Outline each blood parasite and name the species.
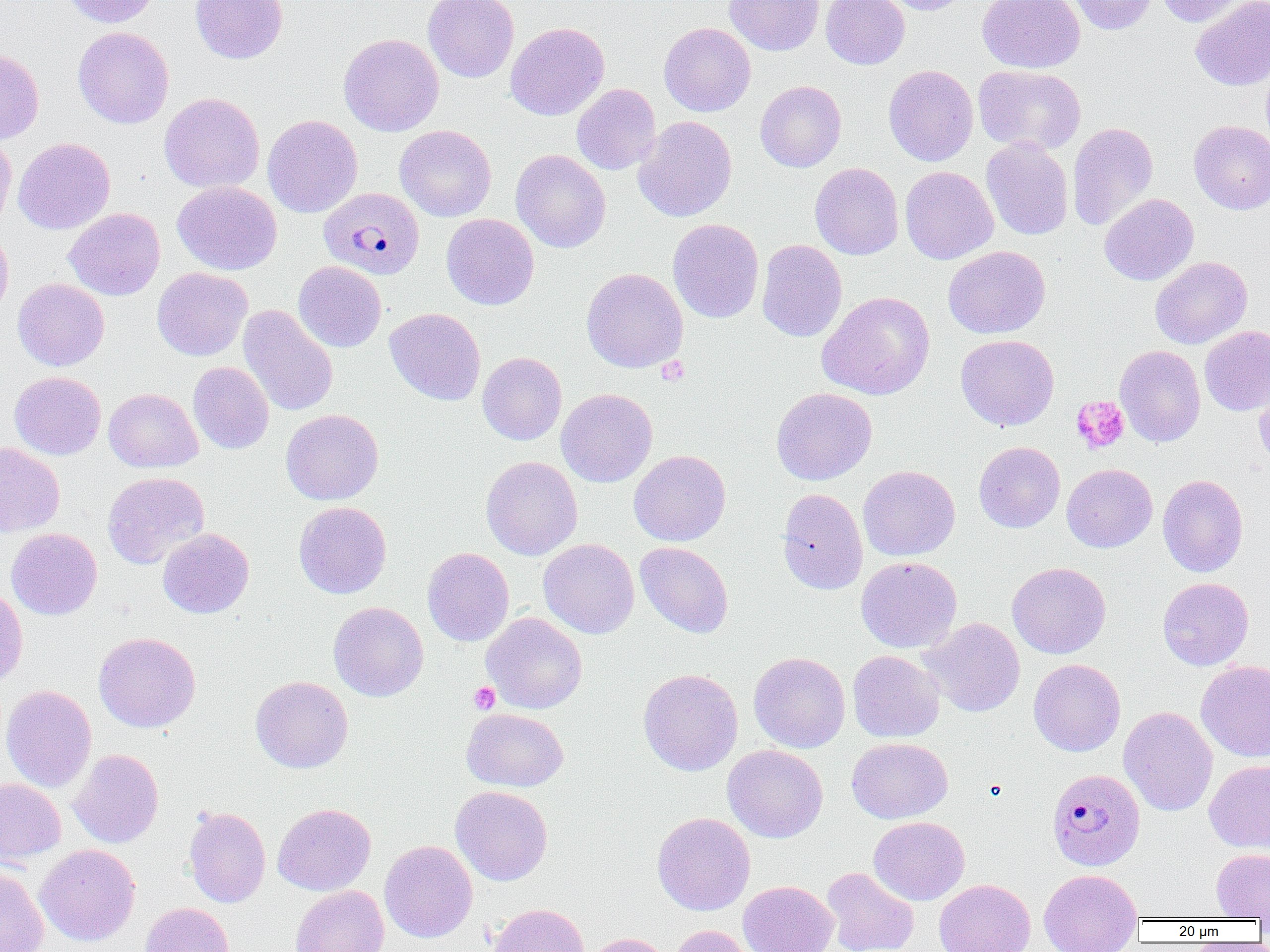

Approximate bounding boxes as named x1/y1/x2/y2 corners in pixels.
Plasmodium malariae-infected red blood cells: (x1=319, y1=187, x2=424, y2=280), (x1=1047, y1=768, x2=1145, y2=871).
No Plasmodium falciparum, Plasmodium ovale, Plasmodium vivax, Babesia divergens, or Trypanosoma brucei observed.

Summary:
  - Uninfected red blood cell locations: (x1=61, y1=0, x2=160, y2=27), (x1=190, y1=0, x2=288, y2=63), (x1=423, y1=0, x2=519, y2=82), (x1=725, y1=0, x2=824, y2=56), (x1=820, y1=0, x2=910, y2=69), (x1=877, y1=0, x2=973, y2=15), (x1=977, y1=0, x2=1085, y2=73), (x1=1065, y1=0, x2=1157, y2=35), (x1=1154, y1=0, x2=1250, y2=26), (x1=1190, y1=1, x2=1270, y2=90), (x1=505, y1=22, x2=610, y2=121), (x1=659, y1=22, x2=756, y2=117), (x1=73, y1=26, x2=174, y2=129), (x1=338, y1=33, x2=444, y2=136), (x1=0, y1=48, x2=44, y2=144), (x1=1261, y1=55, x2=1270, y2=152), (x1=883, y1=64, x2=978, y2=166), (x1=974, y1=64, x2=1086, y2=155), (x1=755, y1=81, x2=846, y2=172), (x1=571, y1=83, x2=661, y2=175), (x1=159, y1=93, x2=264, y2=192), (x1=262, y1=115, x2=362, y2=218), (x1=633, y1=115, x2=737, y2=222), (x1=1189, y1=120, x2=1270, y2=214), (x1=1067, y1=122, x2=1158, y2=231), (x1=395, y1=125, x2=496, y2=222), (x1=0, y1=133, x2=16, y2=232), (x1=12, y1=137, x2=115, y2=235), (x1=981, y1=137, x2=1073, y2=240), (x1=511, y1=149, x2=611, y2=252), (x1=810, y1=162, x2=904, y2=260), (x1=900, y1=166, x2=998, y2=265), (x1=172, y1=181, x2=282, y2=275), (x1=1099, y1=193, x2=1199, y2=285), (x1=64, y1=208, x2=165, y2=300), (x1=441, y1=213, x2=539, y2=310), (x1=667, y1=218, x2=764, y2=324), (x1=0, y1=226, x2=13, y2=322), (x1=757, y1=239, x2=847, y2=342), (x1=943, y1=245, x2=1050, y2=339), (x1=1150, y1=256, x2=1252, y2=349), (x1=293, y1=261, x2=387, y2=352), (x1=152, y1=267, x2=252, y2=361), (x1=581, y1=267, x2=688, y2=373), (x1=12, y1=278, x2=109, y2=371), (x1=817, y1=291, x2=935, y2=400), (x1=239, y1=305, x2=338, y2=416), (x1=385, y1=308, x2=486, y2=405), (x1=1199, y1=325, x2=1270, y2=416), (x1=955, y1=334, x2=1059, y2=431), (x1=1115, y1=345, x2=1205, y2=447), (x1=477, y1=352, x2=567, y2=445), (x1=188, y1=361, x2=274, y2=454), (x1=9, y1=371, x2=106, y2=460), (x1=1254, y1=374, x2=1270, y2=474), (x1=771, y1=387, x2=877, y2=485), (x1=103, y1=388, x2=203, y2=472), (x1=556, y1=388, x2=658, y2=487), (x1=281, y1=409, x2=383, y2=505), (x1=974, y1=441, x2=1065, y2=533), (x1=0, y1=442, x2=65, y2=537), (x1=629, y1=450, x2=730, y2=546), (x1=481, y1=456, x2=583, y2=560), (x1=1062, y1=463, x2=1157, y2=552), (x1=858, y1=465, x2=960, y2=561), (x1=102, y1=471, x2=209, y2=569), (x1=1157, y1=474, x2=1248, y2=577), (x1=777, y1=488, x2=868, y2=595), (x1=293, y1=501, x2=392, y2=599), (x1=6, y1=528, x2=102, y2=620), (x1=157, y1=528, x2=254, y2=618), (x1=538, y1=538, x2=639, y2=638), (x1=634, y1=541, x2=734, y2=638), (x1=422, y1=547, x2=514, y2=647), (x1=855, y1=556, x2=962, y2=653), (x1=1007, y1=562, x2=1111, y2=659), (x1=1157, y1=577, x2=1254, y2=670), (x1=0, y1=586, x2=28, y2=688), (x1=329, y1=601, x2=428, y2=701), (x1=482, y1=612, x2=587, y2=714), (x1=920, y1=618, x2=1025, y2=717), (x1=93, y1=632, x2=201, y2=732), (x1=847, y1=650, x2=945, y2=742), (x1=749, y1=651, x2=850, y2=753), (x1=1028, y1=659, x2=1125, y2=756), (x1=1195, y1=661, x2=1270, y2=762), (x1=638, y1=668, x2=743, y2=776), (x1=250, y1=675, x2=353, y2=773), (x1=1, y1=684, x2=96, y2=793), (x1=1118, y1=706, x2=1218, y2=816), (x1=461, y1=707, x2=569, y2=791), (x1=846, y1=737, x2=953, y2=824), (x1=723, y1=744, x2=828, y2=842), (x1=68, y1=749, x2=164, y2=848), (x1=1204, y1=760, x2=1270, y2=853), (x1=0, y1=777, x2=65, y2=865), (x1=451, y1=785, x2=553, y2=885), (x1=272, y1=803, x2=376, y2=895), (x1=183, y1=806, x2=270, y2=907), (x1=652, y1=812, x2=755, y2=916), (x1=869, y1=816, x2=969, y2=905), (x1=379, y1=840, x2=478, y2=943), (x1=35, y1=844, x2=140, y2=945), (x1=1211, y1=848, x2=1270, y2=920), (x1=0, y1=865, x2=49, y2=952), (x1=822, y1=867, x2=919, y2=952), (x1=1038, y1=868, x2=1143, y2=952), (x1=934, y1=878, x2=1035, y2=952), (x1=739, y1=881, x2=837, y2=952), (x1=290, y1=885, x2=389, y2=952), (x1=139, y1=902, x2=234, y2=952), (x1=487, y1=903, x2=591, y2=952), (x1=668, y1=924, x2=757, y2=952), (x1=581, y1=933, x2=673, y2=952)
  - Platelet locations: (x1=656, y1=357, x2=689, y2=386), (x1=1071, y1=396, x2=1129, y2=454), (x1=469, y1=682, x2=500, y2=714)
  - Slide-level diagnosis: Plasmodium malariae
  - Magnification: 1000x
  - Modality: optical microscopy
  - Field of view: single
  - Preparation: thin blood film
  - Image size: 1270×952 pixels